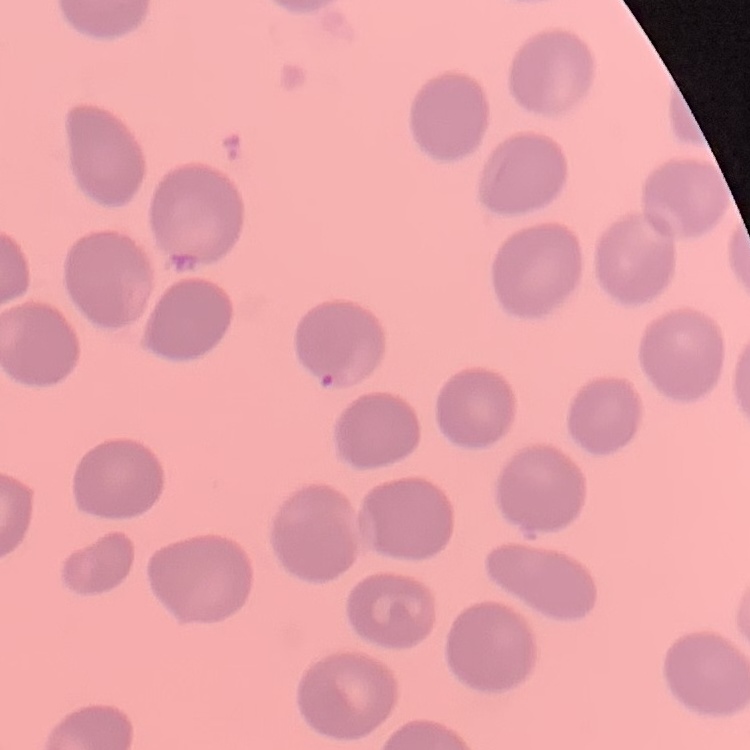
erythrocyte morphology = no rouleaux formation
stain = Field's or Giemsa
image type = square crop of a larger photomicrograph
preparation = thin blood film